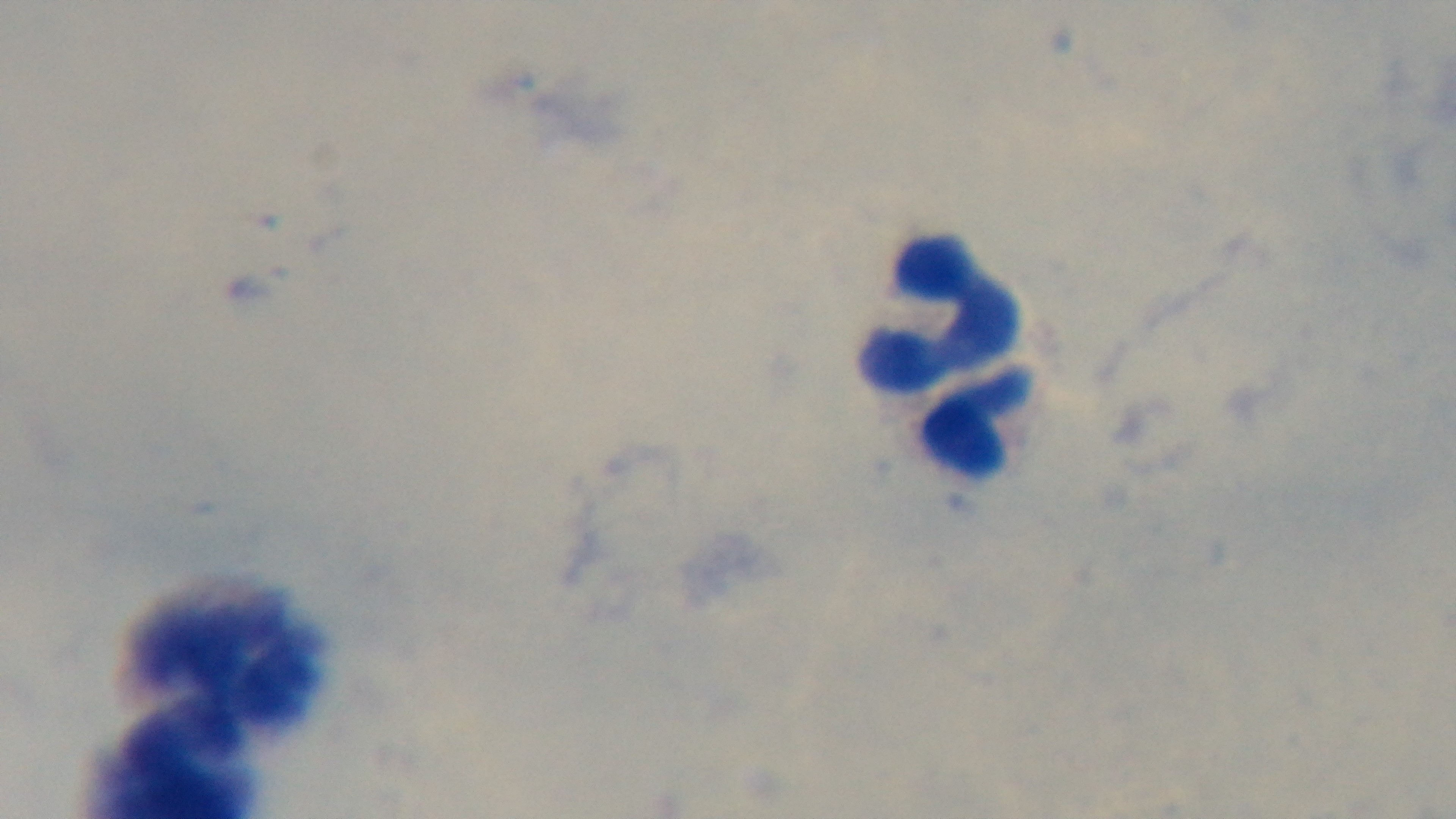 Giemsa-stained. 100x oil-immersion objective. Malaria status: negative. Mounted 4K digital camera. One field from the slide. Preparation: thick smear. Photomicrograph.